Point out each Plasmodium parasite.
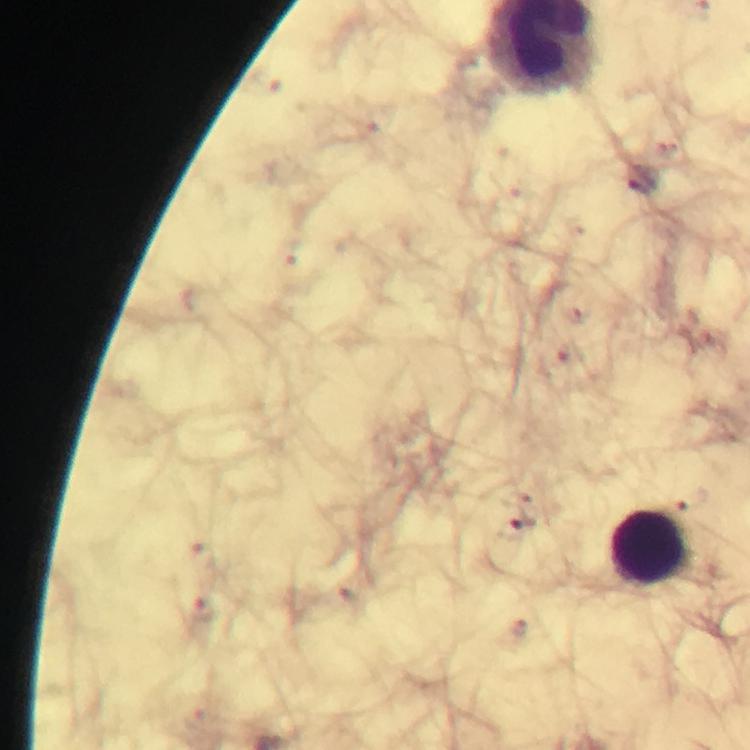

Approximate object centers, in pixels from the top-left corner.
Plasmodium parasites: (x=641, y=180), (x=517, y=529).

Summary:
  - Leukocyte locations: (x=655, y=549)
  - Image size: 750×750 pixels
  - Cropped from: a single field of view
  - Capture: smartphone camera through the microscope
  - Stain: Giemsa
  - Preparation: thick blood film
  - Immersion oil: applied
  - Context: from a malaria diagnostic workup
  - Magnification: 100x